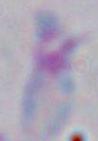

magnification = 1000x
identification = Toxoplasma gondii
modality = photomicrograph